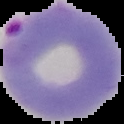

Summary:
  - Image size: 124×124 pixels
  - Result: Plasmodium parasites identified
  - Image type: segmented cell region on a black background
  - Preparation: thin blood smear